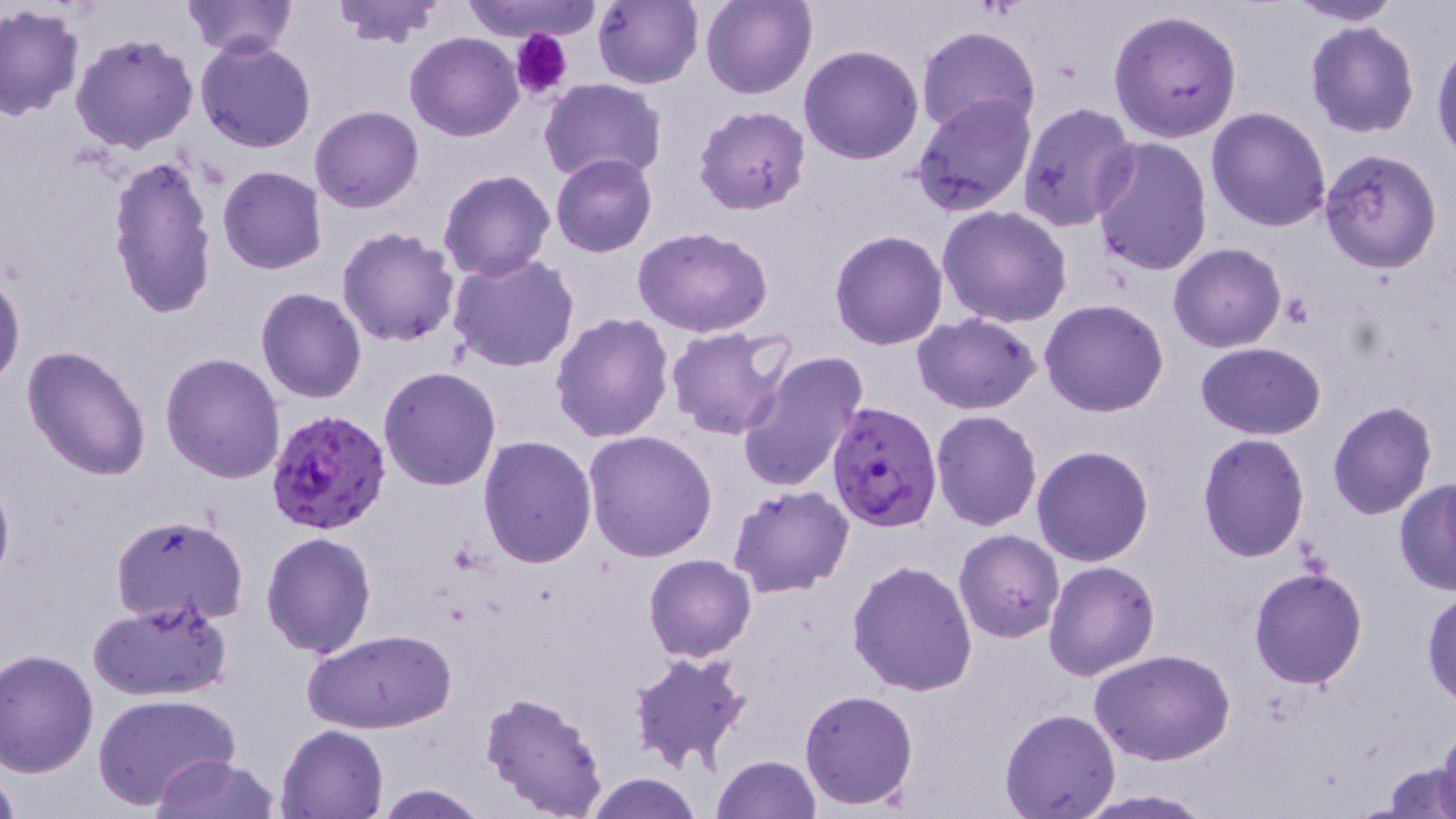

{
  "slide_level_diagnosis": "Plasmodium falciparum",
  "platelet_locations": "approximate bounding boxes as named x1/y1/x2/y2 corners in pixels: (x1=510, y1=29, x2=573, y2=99), (x1=1282, y1=292, x2=1314, y2=328)",
  "plasmodium_falciparum_infected_red_blood_cell_locations": "approximate bounding boxes as named x1/y1/x2/y2 corners in pixels: (x1=823, y1=402, x2=943, y2=532), (x1=265, y1=408, x2=392, y2=539)",
  "stain": "May-Grünwald-Giemsa",
  "preparation": "thin blood smear",
  "image_size": "1456×819 pixels",
  "magnification": "1000x",
  "modality": "optical microscopy",
  "uninfected_red_blood_cell_locations": "approximate bounding boxes as named x1/y1/x2/y2 corners in pixels: (x1=328, y1=0, x2=448, y2=48), (x1=457, y1=0, x2=603, y2=42), (x1=592, y1=0, x2=702, y2=89), (x1=701, y1=0, x2=816, y2=100), (x1=1279, y1=0, x2=1408, y2=25), (x1=180, y1=1, x2=297, y2=56), (x1=0, y1=4, x2=84, y2=118), (x1=1107, y1=8, x2=1242, y2=143), (x1=1304, y1=22, x2=1419, y2=137), (x1=915, y1=25, x2=1041, y2=135), (x1=407, y1=32, x2=524, y2=142), (x1=71, y1=33, x2=200, y2=153), (x1=194, y1=38, x2=317, y2=153), (x1=1432, y1=39, x2=1456, y2=161), (x1=799, y1=45, x2=925, y2=165), (x1=540, y1=78, x2=667, y2=184), (x1=911, y1=93, x2=1037, y2=217), (x1=1017, y1=101, x2=1140, y2=232), (x1=694, y1=104, x2=811, y2=214), (x1=310, y1=105, x2=423, y2=212), (x1=1206, y1=106, x2=1332, y2=230), (x1=1090, y1=138, x2=1213, y2=277), (x1=1317, y1=148, x2=1443, y2=273), (x1=550, y1=153, x2=657, y2=257), (x1=105, y1=154, x2=219, y2=319), (x1=217, y1=165, x2=327, y2=275), (x1=437, y1=168, x2=555, y2=282), (x1=937, y1=204, x2=1072, y2=329), (x1=336, y1=226, x2=462, y2=347), (x1=632, y1=227, x2=774, y2=337), (x1=829, y1=230, x2=947, y2=350), (x1=1169, y1=243, x2=1285, y2=351), (x1=449, y1=254, x2=581, y2=372), (x1=0, y1=269, x2=25, y2=392), (x1=256, y1=287, x2=367, y2=403), (x1=1040, y1=299, x2=1170, y2=418), (x1=551, y1=313, x2=675, y2=444), (x1=911, y1=313, x2=1040, y2=414), (x1=668, y1=326, x2=796, y2=442), (x1=1195, y1=342, x2=1325, y2=439), (x1=21, y1=346, x2=151, y2=482), (x1=736, y1=350, x2=870, y2=492), (x1=160, y1=351, x2=286, y2=482), (x1=379, y1=366, x2=502, y2=491), (x1=1327, y1=401, x2=1436, y2=519), (x1=931, y1=409, x2=1043, y2=531), (x1=583, y1=430, x2=717, y2=561), (x1=1197, y1=434, x2=1311, y2=562), (x1=478, y1=436, x2=598, y2=570), (x1=1031, y1=445, x2=1155, y2=566), (x1=0, y1=471, x2=13, y2=595), (x1=1393, y1=479, x2=1456, y2=595), (x1=728, y1=485, x2=856, y2=599), (x1=111, y1=514, x2=249, y2=625), (x1=953, y1=528, x2=1064, y2=643), (x1=261, y1=532, x2=378, y2=659), (x1=950, y1=544, x2=1157, y2=663), (x1=643, y1=553, x2=755, y2=662), (x1=846, y1=559, x2=977, y2=697), (x1=1043, y1=561, x2=1160, y2=680), (x1=1246, y1=567, x2=1368, y2=689), (x1=1422, y1=588, x2=1456, y2=707), (x1=86, y1=600, x2=232, y2=702), (x1=303, y1=629, x2=456, y2=734), (x1=0, y1=648, x2=100, y2=776), (x1=627, y1=648, x2=753, y2=773), (x1=1091, y1=648, x2=1237, y2=766), (x1=799, y1=688, x2=920, y2=810), (x1=479, y1=691, x2=610, y2=818), (x1=93, y1=693, x2=242, y2=809), (x1=999, y1=708, x2=1121, y2=818), (x1=276, y1=722, x2=389, y2=818), (x1=1436, y1=725, x2=1456, y2=819), (x1=152, y1=754, x2=278, y2=818), (x1=712, y1=756, x2=821, y2=819), (x1=1384, y1=757, x2=1456, y2=818), (x1=0, y1=766, x2=20, y2=819), (x1=582, y1=774, x2=704, y2=818), (x1=372, y1=783, x2=491, y2=817), (x1=1075, y1=790, x2=1218, y2=817)",
  "field_of_view": "single"
}